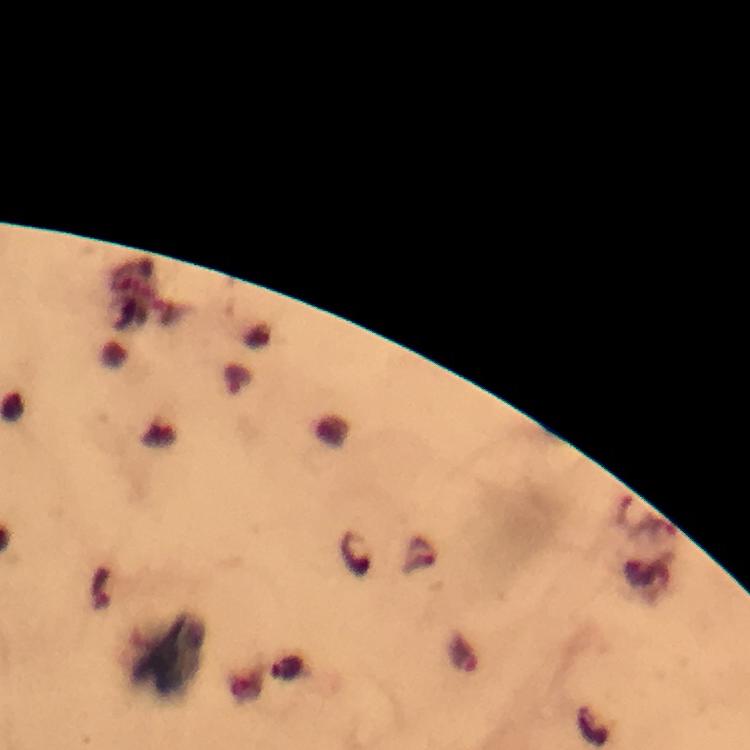

Approximate centers as {x, y} in pixels.
Summary:
  - Plasmodium parasite locations: {239, 380}
  - Image size: 750×750 pixels
  - Magnification: 100x
  - Context: from a diagnostic examination for malaria
  - Immersion oil: applied
  - Cropped from: a single field of view
  - Stain: Giemsa
  - Capture: smartphone photograph through a microscope
  - Preparation: thick smear